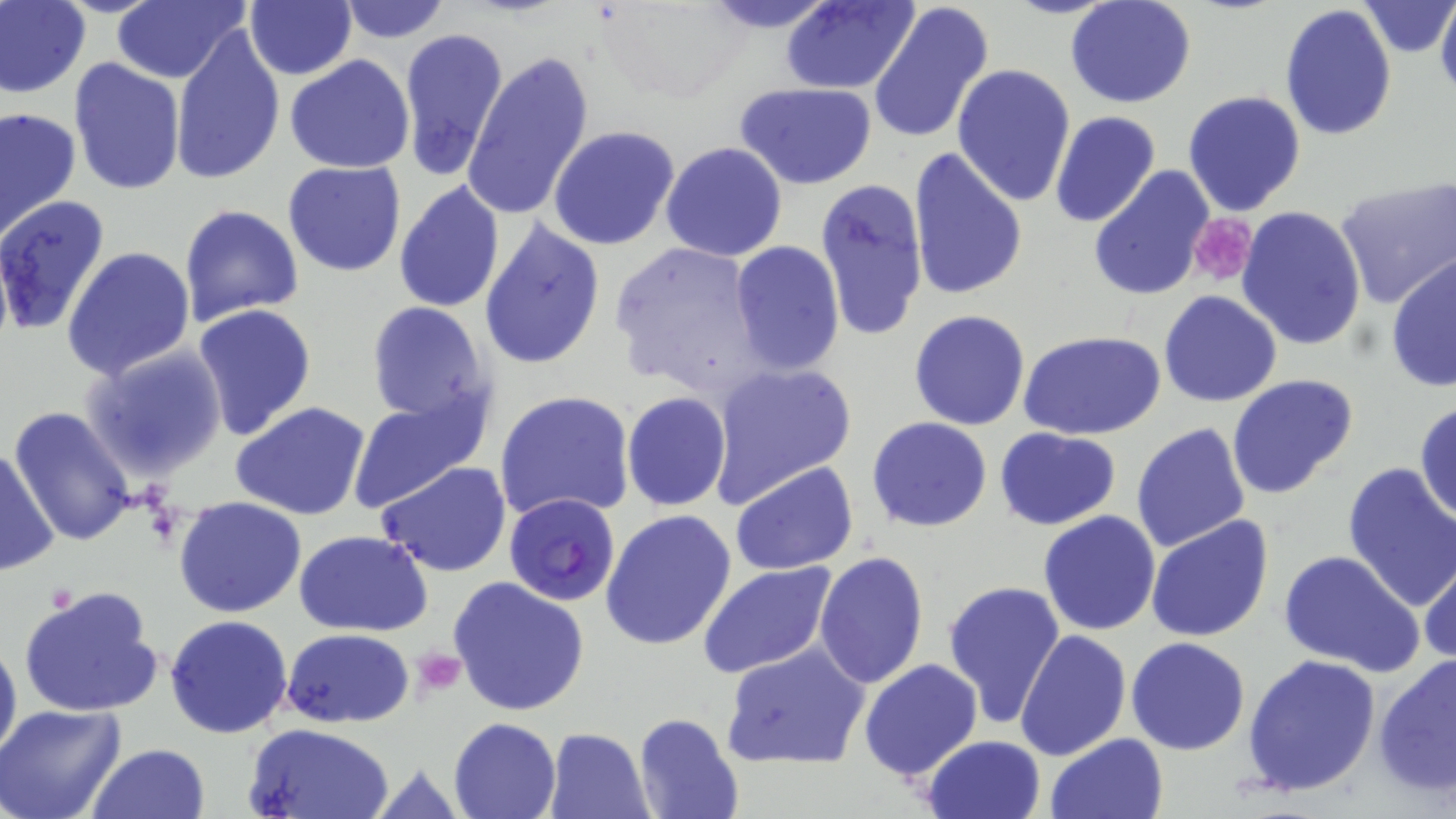

Summary:
  - Coordinate format: approximate bounding boxes as [x1, y1, x2, y2] in pixels
  - Platelet locations: [1187, 215, 1258, 287], [412, 647, 467, 697]
  - Plasmodium falciparum-infected red blood cell locations: [504, 493, 620, 606]
  - Uninfected red blood cell locations: [109, 0, 250, 84], [693, 0, 844, 33], [780, 0, 919, 95], [1004, 0, 1123, 19], [1066, 0, 1198, 109], [1436, 0, 1456, 99], [0, 1, 91, 98], [333, 1, 453, 44], [870, 1, 994, 145], [245, 2, 358, 80], [1361, 2, 1454, 57], [604, 3, 749, 102], [1279, 5, 1397, 141], [169, 22, 286, 186], [397, 27, 508, 182], [462, 51, 593, 220], [285, 54, 415, 173], [69, 57, 185, 195], [951, 63, 1076, 206], [737, 82, 879, 188], [1183, 88, 1308, 215], [0, 104, 81, 240], [1049, 110, 1161, 228], [548, 124, 680, 250], [660, 143, 787, 262], [907, 146, 1028, 302], [282, 161, 407, 278], [1087, 166, 1216, 302], [813, 178, 928, 343], [1335, 178, 1456, 308], [391, 180, 505, 316], [0, 195, 111, 336], [179, 204, 304, 326], [1235, 205, 1368, 350], [477, 217, 606, 372], [608, 238, 769, 399], [729, 241, 845, 375], [63, 245, 196, 382], [1386, 255, 1456, 393], [1158, 290, 1284, 407], [365, 302, 491, 427], [191, 304, 317, 442], [908, 308, 1031, 430], [1019, 330, 1167, 441], [81, 346, 229, 482], [705, 360, 856, 503], [1227, 373, 1358, 501], [495, 390, 635, 524], [347, 392, 490, 511], [620, 392, 732, 510], [1414, 400, 1456, 523], [229, 401, 372, 519], [9, 407, 138, 546], [866, 416, 994, 533], [1131, 423, 1251, 553], [994, 426, 1122, 530], [0, 445, 59, 581], [375, 461, 514, 579], [730, 461, 857, 576], [1342, 461, 1456, 612], [172, 496, 307, 619], [600, 509, 736, 653], [1039, 510, 1161, 635], [1146, 515, 1275, 644], [294, 530, 435, 637], [1279, 550, 1426, 677], [813, 551, 927, 691], [1419, 553, 1456, 666], [698, 562, 841, 680], [447, 577, 590, 720], [942, 580, 1067, 732], [19, 584, 166, 719], [164, 614, 293, 738], [0, 627, 21, 769], [280, 627, 414, 729], [1015, 629, 1131, 761], [1126, 636, 1252, 755], [720, 642, 870, 770], [1374, 654, 1456, 796], [1242, 655, 1382, 797], [858, 659, 983, 783], [0, 703, 128, 819], [632, 714, 744, 819], [448, 717, 561, 819], [244, 722, 396, 819], [544, 727, 654, 818], [1045, 733, 1168, 819], [920, 735, 1047, 819], [86, 743, 212, 819], [361, 756, 471, 818]
  - Slide-level diagnosis: Plasmodium falciparum
  - Modality: light microscopy
  - Image size: 1456×819 pixels
  - Stain: May-Grünwald-Giemsa
  - Magnification: 1000x
  - Field of view: single
  - Preparation: thin blood smear